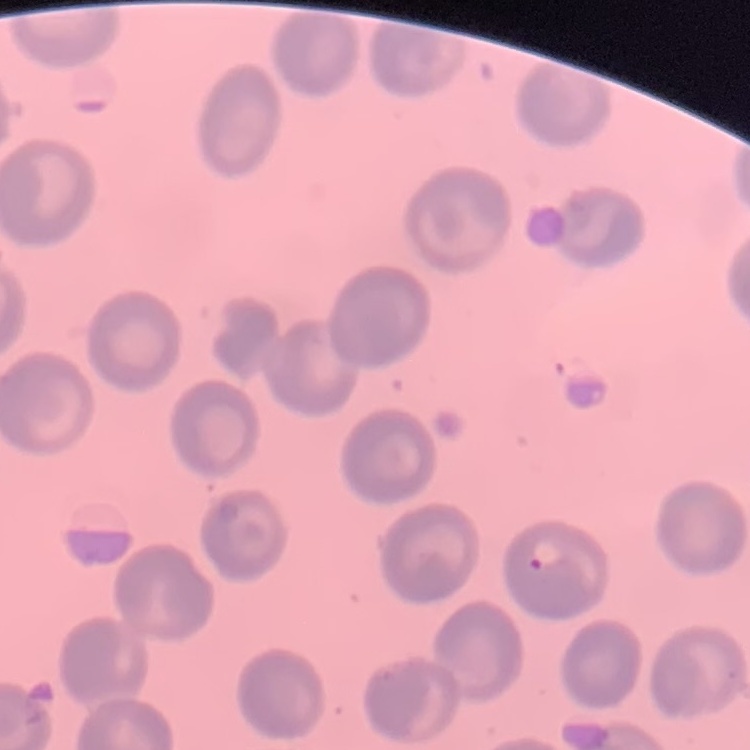
Summary:
  - Red blood cell morphology: no rouleaux formation
  - Image type: one tile cut from a larger photomicrograph
  - Preparation: thin peripheral smear
  - Stain: Field's or Giemsa